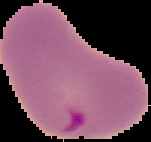

Summary:
  - Image size: 151×142 pixels
  - Image type: segmented cell region with the area outside set to black
  - Preparation: thin blood film
  - Malaria status: parasitized